Classify this cell by malaria status.
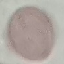
It is uninfected.

image type = automatically extracted cell patch, resized to 64 × 64 pixels
stain = Giemsa
capture = smartphone camera at the microscope eyepiece
preparation = thin smear